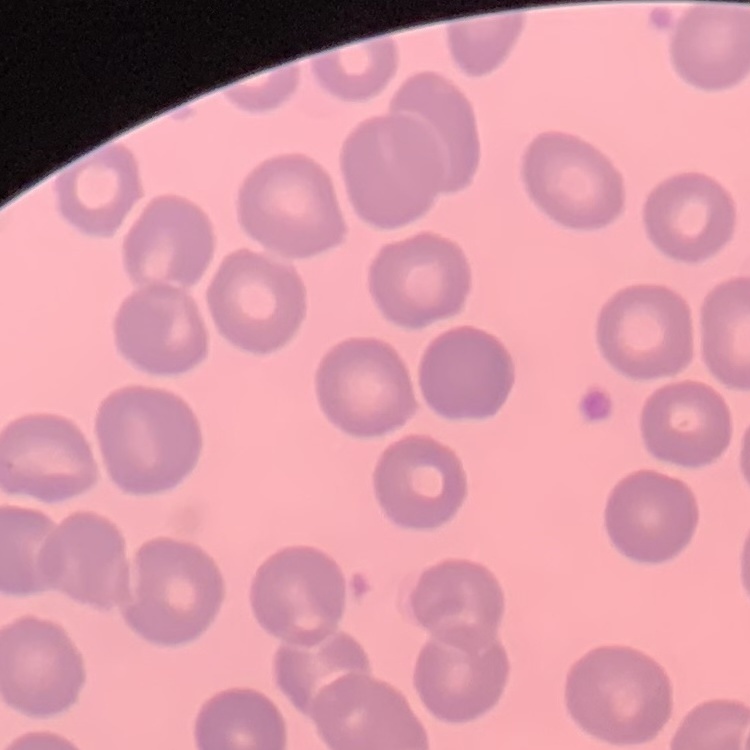

red_blood_cell_morphology: no rouleaux formation
preparation: thin blood smear
image_type: one tile cut from a larger photomicrograph
stain: Field's or Giemsa